Classify this cell by malaria status.
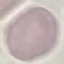

Uninfected.

image type = cell patch, automatically extracted from a larger field of view and resized to 64 × 64 pixels
stain = Giemsa
capture = smartphone camera at the microscope eyepiece
preparation = thin blood film